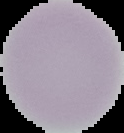 The area outside the segmented cell region is set to black. Image is 124×133 pixels. Malaria status: uninfected. From a thin blood smear.